Name the parasite shown.
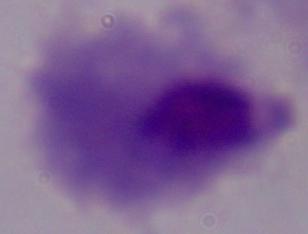

This is a trichomonad.

Summary:
  - Magnification: 1000x
  - Modality: photomicrograph